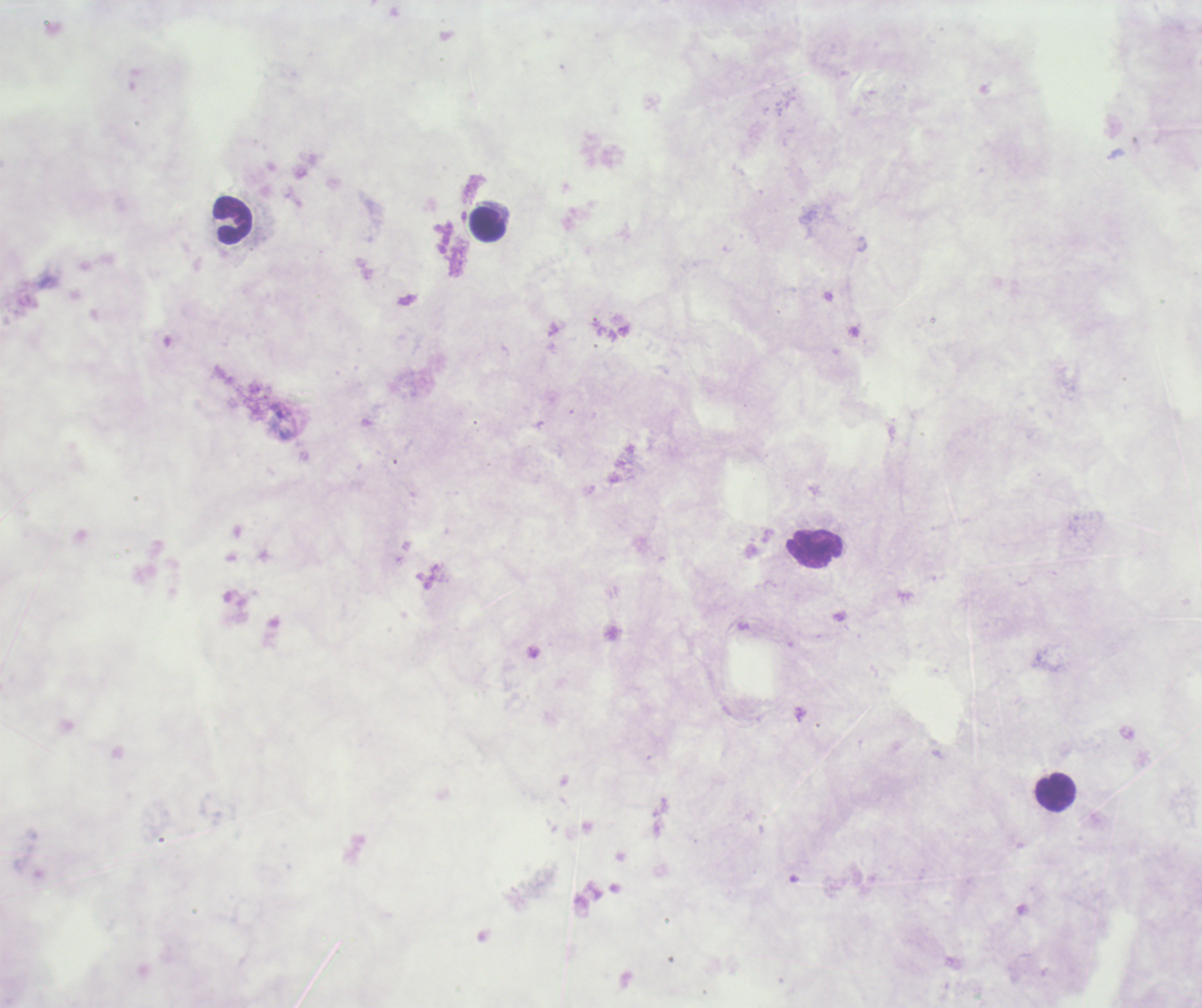
Approximate centers as [x, y] in pixels. Leukocyte locations: [231, 220], [488, 224], [815, 550], [1054, 791]. Romanowsky stain. Image is 1202×1008 pixels. Previously used in a real diagnosis. One field from this slide. Thick blood film. Captured at 100x magnification. Coloration quality: bad. Result: no malaria parasites detected. Background quality: unsatisfactory.